Assess this cell for malaria.
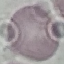
Uninfected.

Thin blood film. Acquired by smartphone through the microscope eyepiece. Automatically extracted cell patch, resized to 64 × 64 pixels. Giemsa-stained preparation.